Find each parasitized RBC.
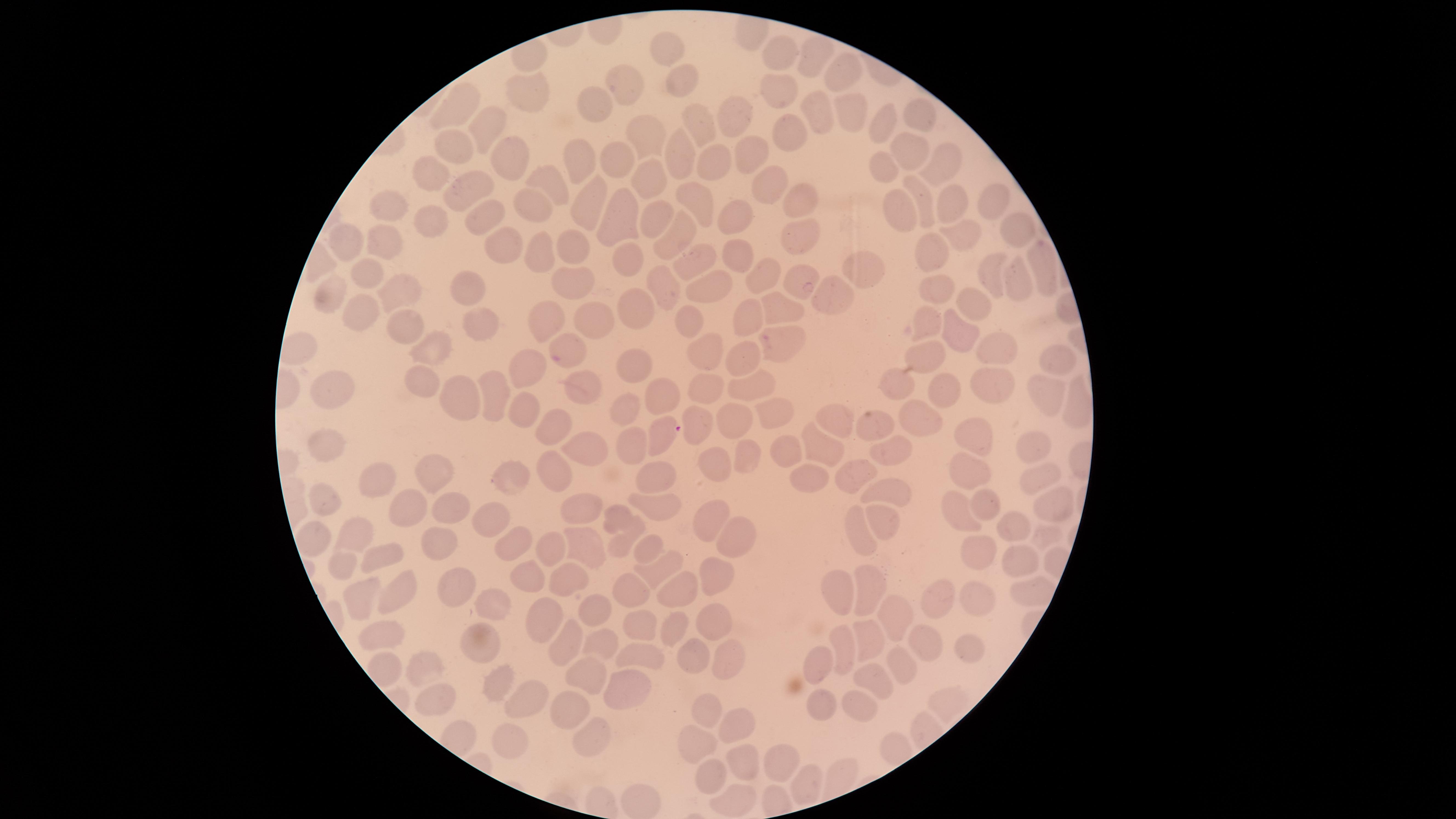
Approximate marker points, in pixels from the top-left corner.
Parasitized RBCs: (x=766, y=339), (x=556, y=359), (x=670, y=428).

image size = 1456×819 pixels
preparation = thin blood film
visible region = circular
stain = Giemsa
capture = smartphone photograph through the microscope eyepiece
field of view = single
uninfected RBCs = approximate marker points, in pixels from the top-left corner: (x=670, y=52), (x=785, y=52), (x=815, y=53), (x=847, y=75), (x=628, y=85), (x=681, y=87), (x=780, y=88), (x=535, y=90), (x=458, y=102), (x=598, y=107), (x=850, y=110), (x=915, y=113), (x=816, y=115), (x=732, y=117), (x=491, y=123), (x=890, y=125), (x=789, y=127), (x=700, y=133), (x=643, y=140), (x=451, y=143), (x=905, y=154), (x=749, y=155), (x=582, y=158), (x=945, y=158), (x=512, y=159), (x=681, y=159), (x=716, y=160), (x=623, y=163), (x=434, y=171), (x=882, y=171), (x=547, y=179), (x=651, y=183), (x=463, y=185), (x=765, y=190), (x=917, y=197), (x=952, y=197), (x=588, y=198), (x=539, y=200), (x=702, y=200), (x=389, y=202), (x=802, y=202), (x=991, y=203), (x=904, y=211), (x=656, y=212), (x=629, y=214), (x=482, y=215), (x=741, y=215), (x=432, y=220), (x=1014, y=231), (x=970, y=233), (x=681, y=235), (x=383, y=236), (x=803, y=237), (x=353, y=241), (x=510, y=246), (x=543, y=246), (x=576, y=247), (x=928, y=256), (x=631, y=259), (x=739, y=259), (x=699, y=261), (x=1045, y=269), (x=988, y=271), (x=365, y=273), (x=1015, y=273), (x=855, y=275), (x=761, y=278), (x=797, y=279), (x=577, y=281), (x=708, y=283), (x=663, y=285), (x=463, y=288), (x=938, y=292), (x=392, y=293), (x=338, y=294), (x=832, y=295), (x=975, y=305), (x=782, y=307), (x=637, y=308), (x=369, y=312), (x=752, y=319), (x=594, y=320), (x=693, y=323), (x=546, y=325), (x=934, y=325), (x=409, y=328), (x=479, y=330), (x=966, y=337), (x=432, y=348), (x=999, y=351), (x=929, y=353), (x=710, y=359), (x=1051, y=362), (x=739, y=365), (x=635, y=366), (x=531, y=375), (x=428, y=383), (x=895, y=384), (x=585, y=387), (x=338, y=388), (x=757, y=388), (x=710, y=389), (x=989, y=392), (x=1044, y=394), (x=465, y=395), (x=660, y=395), (x=950, y=398), (x=497, y=400), (x=623, y=411), (x=530, y=414), (x=776, y=414), (x=740, y=416), (x=838, y=423), (x=557, y=426), (x=921, y=426), (x=876, y=429), (x=699, y=432), (x=1028, y=439), (x=588, y=442), (x=634, y=444), (x=331, y=445), (x=817, y=445), (x=977, y=445), (x=786, y=447), (x=895, y=447), (x=752, y=451), (x=714, y=464), (x=556, y=467), (x=972, y=471), (x=860, y=472), (x=517, y=473), (x=813, y=474), (x=432, y=477), (x=659, y=477), (x=1042, y=480), (x=373, y=481), (x=894, y=498), (x=1047, y=499), (x=660, y=503), (x=404, y=505), (x=987, y=505), (x=582, y=508), (x=330, y=509), (x=453, y=509), (x=955, y=512), (x=616, y=515), (x=715, y=515), (x=491, y=517), (x=884, y=519), (x=1010, y=524), (x=858, y=532), (x=357, y=534), (x=734, y=535), (x=1042, y=537), (x=438, y=541), (x=511, y=542), (x=624, y=544), (x=582, y=547), (x=654, y=547), (x=554, y=552), (x=385, y=557), (x=981, y=559), (x=1014, y=560), (x=347, y=567), (x=527, y=570), (x=667, y=572), (x=719, y=576), (x=562, y=580), (x=871, y=587), (x=392, y=591), (x=637, y=591), (x=677, y=591), (x=357, y=592), (x=458, y=594), (x=843, y=600), (x=934, y=601), (x=982, y=601), (x=493, y=609), (x=596, y=609), (x=717, y=619), (x=895, y=619), (x=548, y=624), (x=380, y=625), (x=673, y=629), (x=642, y=630), (x=912, y=639), (x=558, y=640), (x=476, y=641), (x=608, y=642), (x=847, y=645), (x=877, y=645), (x=973, y=647), (x=640, y=654), (x=696, y=657), (x=727, y=659), (x=902, y=660), (x=818, y=664), (x=424, y=671), (x=588, y=673), (x=873, y=676), (x=499, y=684), (x=630, y=692), (x=445, y=698), (x=532, y=702), (x=850, y=702), (x=819, y=705), (x=578, y=714), (x=710, y=714), (x=731, y=726), (x=508, y=735), (x=596, y=740), (x=701, y=740), (x=782, y=762), (x=738, y=767), (x=712, y=776)
species = Plasmodium falciparum